Name the parasite shown.
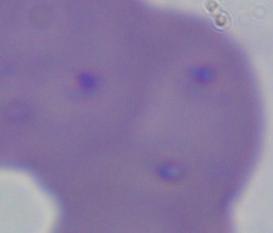
Babesia.

Summary:
  - Magnification: 1000x
  - Modality: micrograph